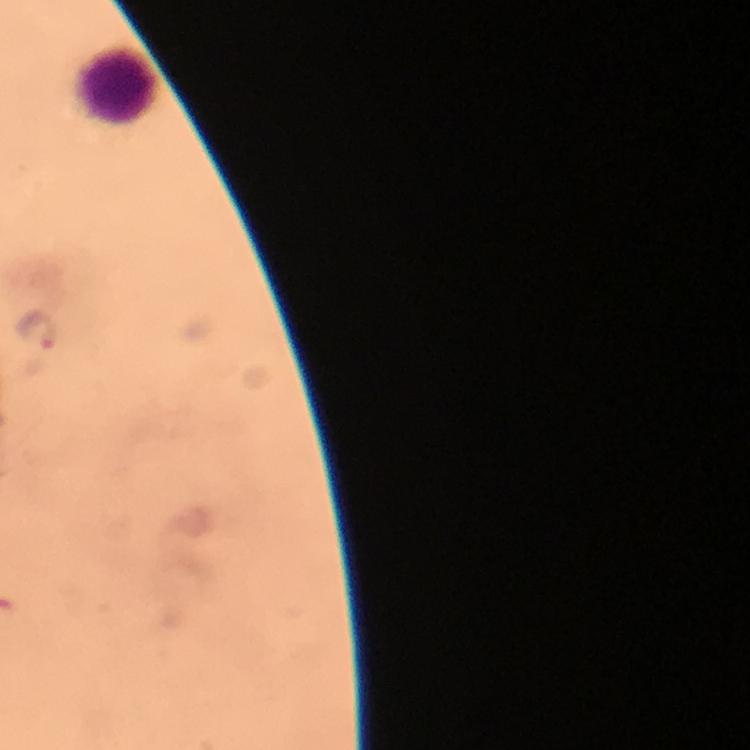

leukocyte_locations: 'approximate object centers, in pixels from the top-left corner: (x=120, y=87)'
preparation: thick blood film
plasmodium_parasite_locations: 'approximate object centers, in pixels from the top-left corner: (x=37, y=328)'
context: from a diagnostic examination for malaria
capture: smartphone camera through the microscope
image_size: 750×750 pixels
stain: Giemsa
cropped_from: one field of view
immersion_oil: used
magnification: 100x